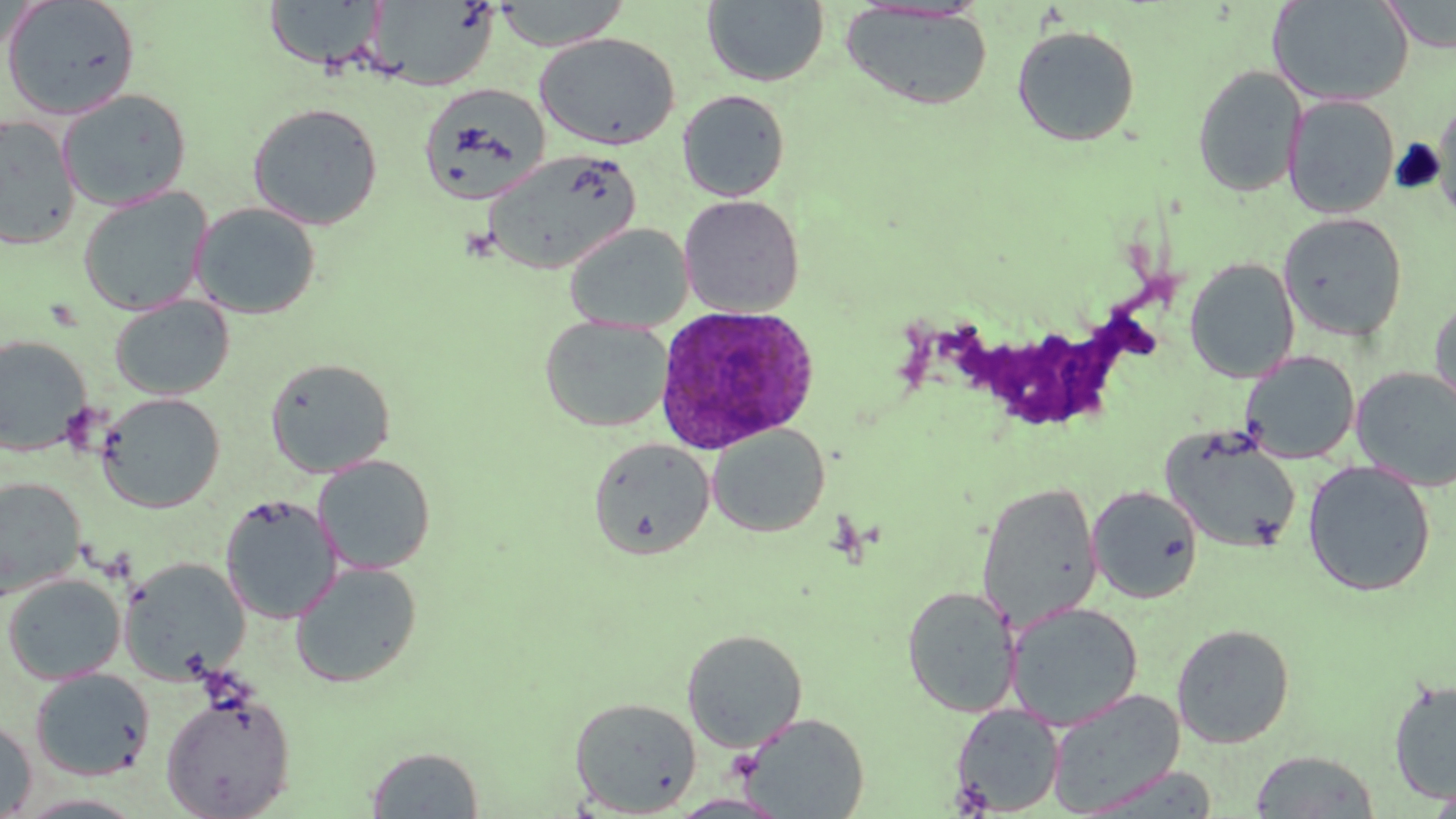

Approximate bounding boxes as (x1,y1)-(x2,y2) corner pairs in pixels. Plasmodium ovale-infected red blood cell locations: (653,304)-(819,454). Platelet locations: (949,778)-(995,817). Uninfected red blood cell locations: (1,0)-(142,120), (367,0)-(499,91), (493,0)-(630,51), (703,0)-(829,87), (1381,0)-(1456,52), (263,1)-(387,72), (1268,1)-(1414,106), (842,3)-(993,111), (1011,25)-(1140,146), (535,32)-(680,150), (1192,65)-(1307,197), (419,82)-(552,204), (57,89)-(193,211), (677,90)-(790,202), (1283,94)-(1400,219), (1433,94)-(1456,228), (247,102)-(383,230), (0,114)-(81,250), (483,149)-(641,275), (77,187)-(213,316), (679,194)-(804,317), (191,201)-(322,319), (1278,212)-(1408,342), (564,223)-(694,333), (1184,257)-(1300,383), (1429,294)-(1456,420), (109,295)-(234,400), (539,315)-(673,432), (0,335)-(93,456), (1240,350)-(1360,464), (265,356)-(396,477), (1351,367)-(1456,490), (97,393)-(225,513), (707,423)-(830,537), (1160,428)-(1302,553), (588,437)-(715,560), (313,454)-(436,575), (1302,460)-(1436,597), (0,477)-(86,601), (976,481)-(1103,630), (1087,485)-(1203,604), (220,495)-(341,624), (119,556)-(252,684), (290,561)-(423,688), (2,573)-(126,684), (902,585)-(1021,718), (1005,601)-(1143,730), (1171,623)-(1295,748), (682,628)-(808,753), (30,667)-(155,781), (1387,679)-(1456,803), (1046,689)-(1185,814), (161,690)-(296,819), (570,696)-(701,816), (950,703)-(1065,815), (736,711)-(870,818), (0,716)-(37,817), (366,746)-(484,818), (1249,750)-(1380,818), (1076,764)-(1219,818), (1421,787)-(1456,817), (668,793)-(790,818). Slide-level diagnosis: Plasmodium ovale. May-Grünwald-Giemsa stain. One field of a larger specimen. Optical microscopy. 1000x magnification. Image is 1456×819 pixels. Thin blood film.